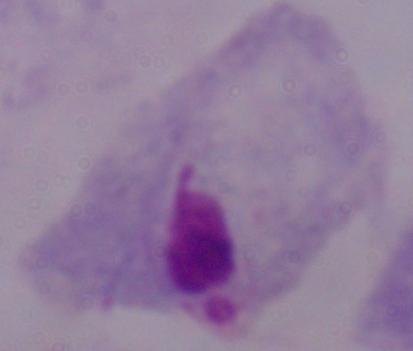

modality = micrograph
magnification = 1000x
identification = trichomonad